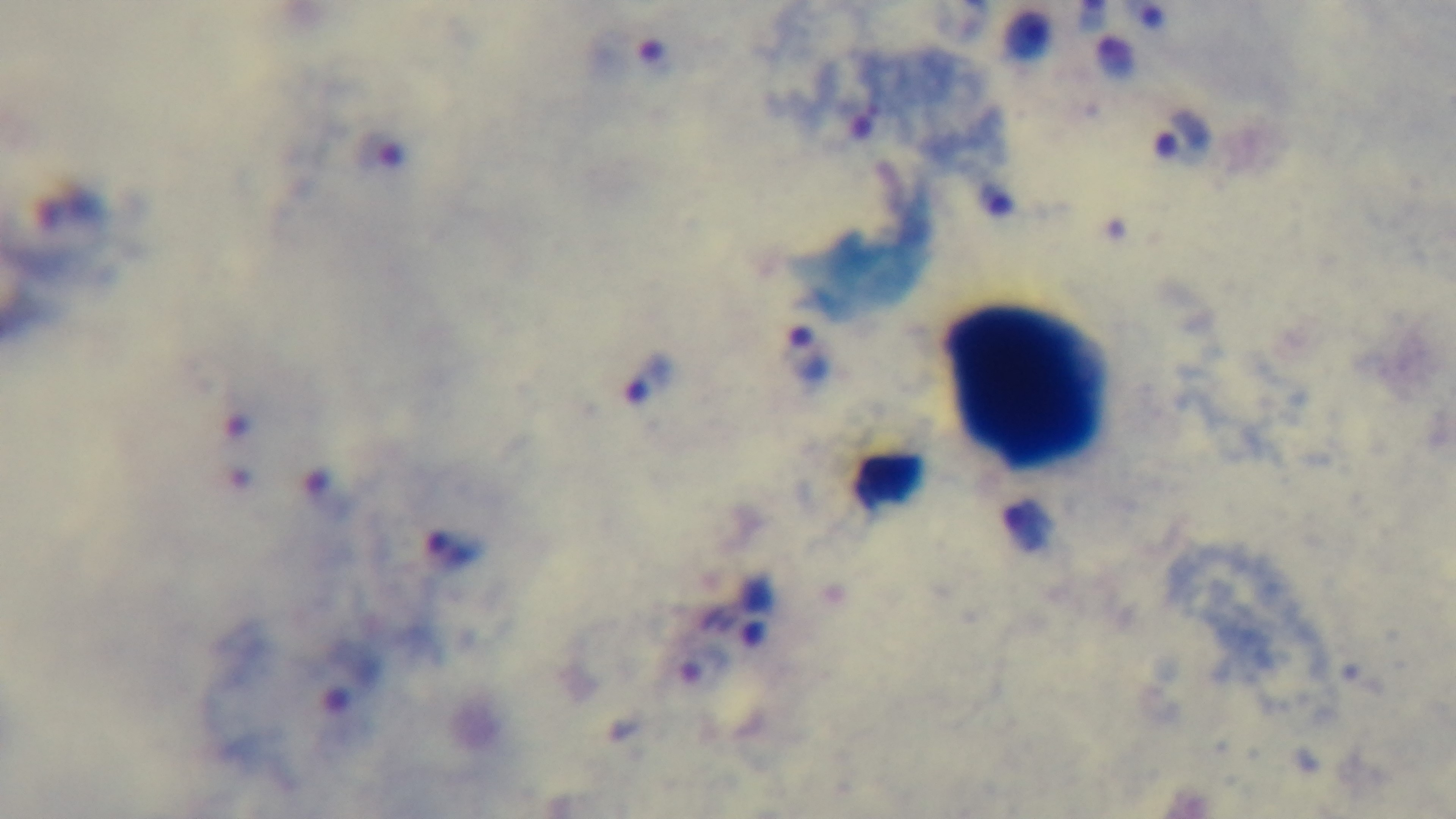

field_of_view: one from the slide
objective: 100x oil immersion
preparation: thick
modality: light microscopy
capture: mounted 4K digital camera
malaria_status: infected
stain: Giemsa